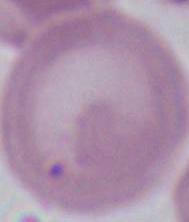
Summary:
  - Magnification: 1000x
  - Modality: photomicrograph
  - Identification: red blood cell